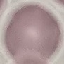 Result: negative for malaria parasites. Acquired by smartphone through the microscope eyepiece. Thin smear of blood. Giemsa-stained preparation. Cell patch, automatically extracted from a larger field of view and resized to 64 × 64 pixels.